Outline each blood parasite and name the species.
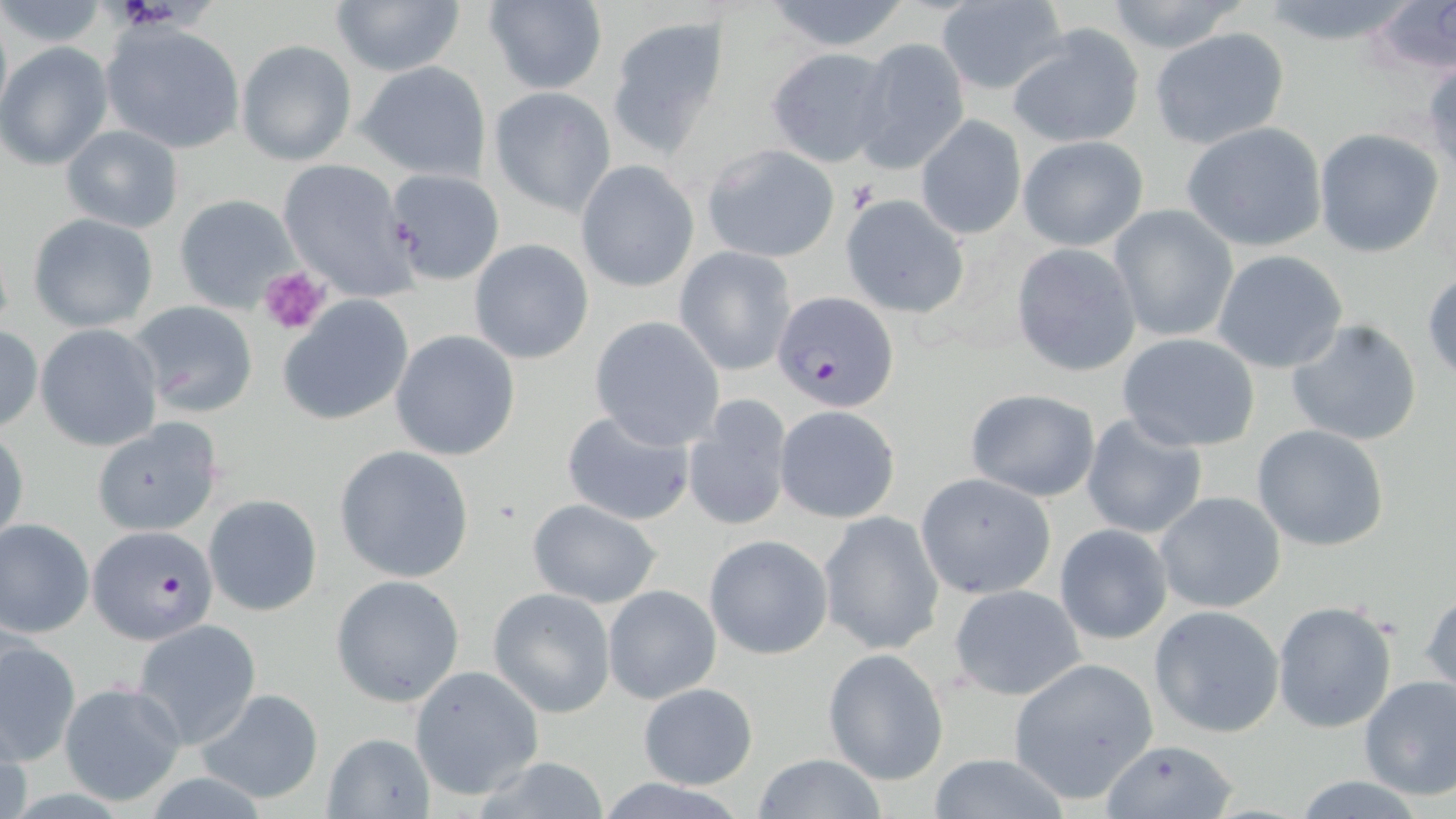
Approximate bounding boxes as (x1,y1)-(x2,y2) corner pairs in pixels.
Plasmodium falciparum-infected red blood cells: (771,290)-(900,413), (86,526)-(219,644).
No Plasmodium ovale, Plasmodium malariae, Plasmodium vivax, Babesia divergens, or Trypanosoma brucei observed.

slide-level diagnosis = Plasmodium falciparum
magnification = 1000x
preparation = thin blood smear
platelet locations = approximate bounding boxes as (x1,y1)-(x2,y2) corner pairs in pixels: (111,0)-(178,26), (259,266)-(329,335)
stain = May-Grünwald-Giemsa
uninfected red blood cell locations = approximate bounding boxes as (x1,y1)-(x2,y2) corner pairs in pixels: (328,0)-(467,76), (1100,0)-(1252,56), (1,1)-(109,50), (482,1)-(607,94), (759,1)-(916,52), (935,1)-(1069,95), (1368,2)-(1456,78), (0,5)-(11,124), (606,15)-(729,158), (100,21)-(246,155), (1008,23)-(1145,148), (1149,27)-(1289,150), (855,37)-(970,175), (236,39)-(357,166), (0,42)-(114,170), (764,47)-(893,166), (357,61)-(490,181), (488,86)-(617,216), (916,115)-(1025,240), (1181,123)-(1327,252), (61,125)-(184,232), (1313,127)-(1445,259), (1016,135)-(1149,252), (702,143)-(840,263), (277,159)-(417,301), (577,161)-(699,291), (384,169)-(504,285), (173,195)-(300,313), (840,195)-(971,321), (1109,205)-(1237,344), (29,214)-(160,332), (469,239)-(594,364), (1010,243)-(1146,378), (673,247)-(797,377), (1212,250)-(1348,374), (1424,271)-(1456,381), (280,296)-(414,425), (128,301)-(259,419), (589,317)-(724,448), (1286,318)-(1423,448), (35,324)-(162,452), (0,326)-(43,434), (390,330)-(521,461), (1116,332)-(1260,452), (964,388)-(1099,501), (683,395)-(796,530), (775,405)-(900,524), (559,409)-(696,524), (1080,411)-(1208,540), (91,417)-(225,537), (1251,423)-(1391,552), (0,426)-(28,551), (334,444)-(476,583), (916,473)-(1056,600), (1154,491)-(1287,613), (205,494)-(323,616), (523,498)-(662,608), (818,512)-(944,654), (0,518)-(96,636), (1054,524)-(1172,645), (704,534)-(834,661), (331,573)-(465,707), (948,583)-(1087,702), (603,584)-(722,703), (1421,586)-(1455,704), (488,588)-(616,716), (1271,600)-(1399,735), (1149,604)-(1285,738), (133,620)-(260,749), (0,634)-(80,767), (822,649)-(948,785), (1007,657)-(1158,804), (410,665)-(544,800), (1358,675)-(1456,803), (58,680)-(188,806), (636,682)-(761,789), (196,688)-(323,804), (322,731)-(435,818), (1097,739)-(1241,819), (928,753)-(1069,819), (752,755)-(885,817), (463,758)-(619,818), (1288,776)-(1438,818)
field of view = single
image size = 1456×819 pixels
modality = light microscopy